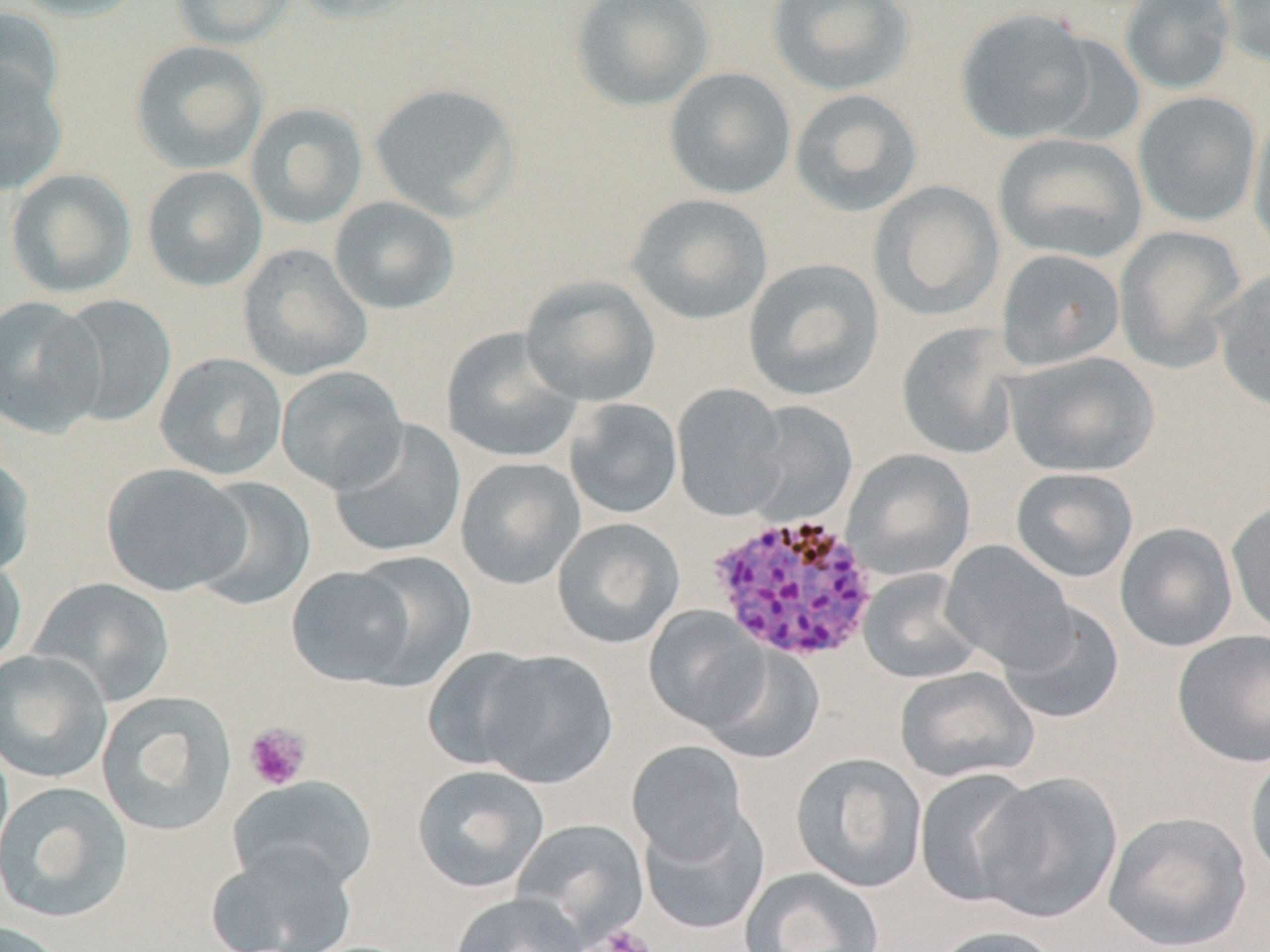
{
  "slide_level_diagnosis": "Plasmodium vivax",
  "modality": "light microscopy",
  "preparation": "thin blood film",
  "magnification": "1000x",
  "image_size": "1270×952 pixels",
  "uninfected_red_blood_cell_locations": "approximate bounding boxes as (x1, y1, x2, y2) in pixels: (10, 0, 151, 22), (171, 0, 297, 50), (287, 0, 428, 25), (570, 0, 715, 111), (766, 0, 916, 96), (1119, 0, 1236, 95), (1220, 0, 1270, 69), (0, 7, 64, 120), (954, 7, 1098, 144), (129, 40, 269, 175), (0, 61, 68, 197), (664, 67, 796, 199), (367, 82, 519, 221), (788, 88, 923, 218), (1132, 91, 1262, 228), (245, 102, 368, 230), (1247, 108, 1270, 257), (993, 133, 1148, 264), (141, 166, 268, 292), (5, 168, 137, 299), (868, 180, 1004, 321), (626, 193, 773, 325), (328, 196, 461, 316), (1113, 226, 1248, 372), (237, 244, 372, 382), (996, 248, 1125, 371), (743, 258, 883, 401), (1213, 267, 1270, 412), (521, 274, 662, 407), (0, 295, 105, 438), (54, 295, 177, 427), (895, 322, 1024, 461), (441, 327, 585, 464), (1004, 351, 1159, 477), (154, 352, 288, 480), (276, 366, 409, 495), (671, 384, 789, 521), (565, 398, 684, 520), (743, 400, 860, 526), (329, 420, 467, 559), (842, 448, 976, 580), (0, 451, 35, 580), (455, 456, 587, 591), (100, 462, 253, 597), (1010, 467, 1139, 583), (189, 476, 317, 612), (1226, 499, 1270, 638), (552, 517, 685, 649), (1115, 522, 1238, 652), (941, 540, 1077, 673), (0, 550, 28, 672), (344, 552, 477, 688), (287, 565, 420, 687), (858, 568, 984, 684), (30, 577, 176, 706), (997, 601, 1125, 724), (644, 608, 770, 732), (1171, 629, 1270, 768), (699, 645, 826, 764), (424, 647, 550, 771), (0, 649, 113, 784), (477, 651, 619, 789), (894, 666, 1038, 784), (96, 690, 238, 837), (626, 740, 749, 864), (1245, 751, 1270, 884), (791, 753, 927, 893), (411, 764, 549, 893), (914, 768, 1040, 907), (975, 771, 1123, 923), (228, 775, 378, 894), (0, 781, 134, 924), (639, 806, 770, 935), (1103, 810, 1253, 951), (510, 817, 650, 943), (205, 844, 358, 952), (740, 867, 885, 952), (449, 892, 590, 952), (0, 920, 71, 952), (929, 925, 1064, 952)",
  "plasmodium_vivax_infected_red_blood_cell_locations": "approximate bounding boxes as (x1, y1, x2, y2) in pixels: (706, 511, 881, 664)",
  "field_of_view": "one of a larger specimen",
  "platelet_locations": "approximate bounding boxes as (x1, y1, x2, y2) in pixels: (244, 723, 311, 791), (593, 925, 657, 952)",
  "stain": "May-Grünwald-Giemsa"
}